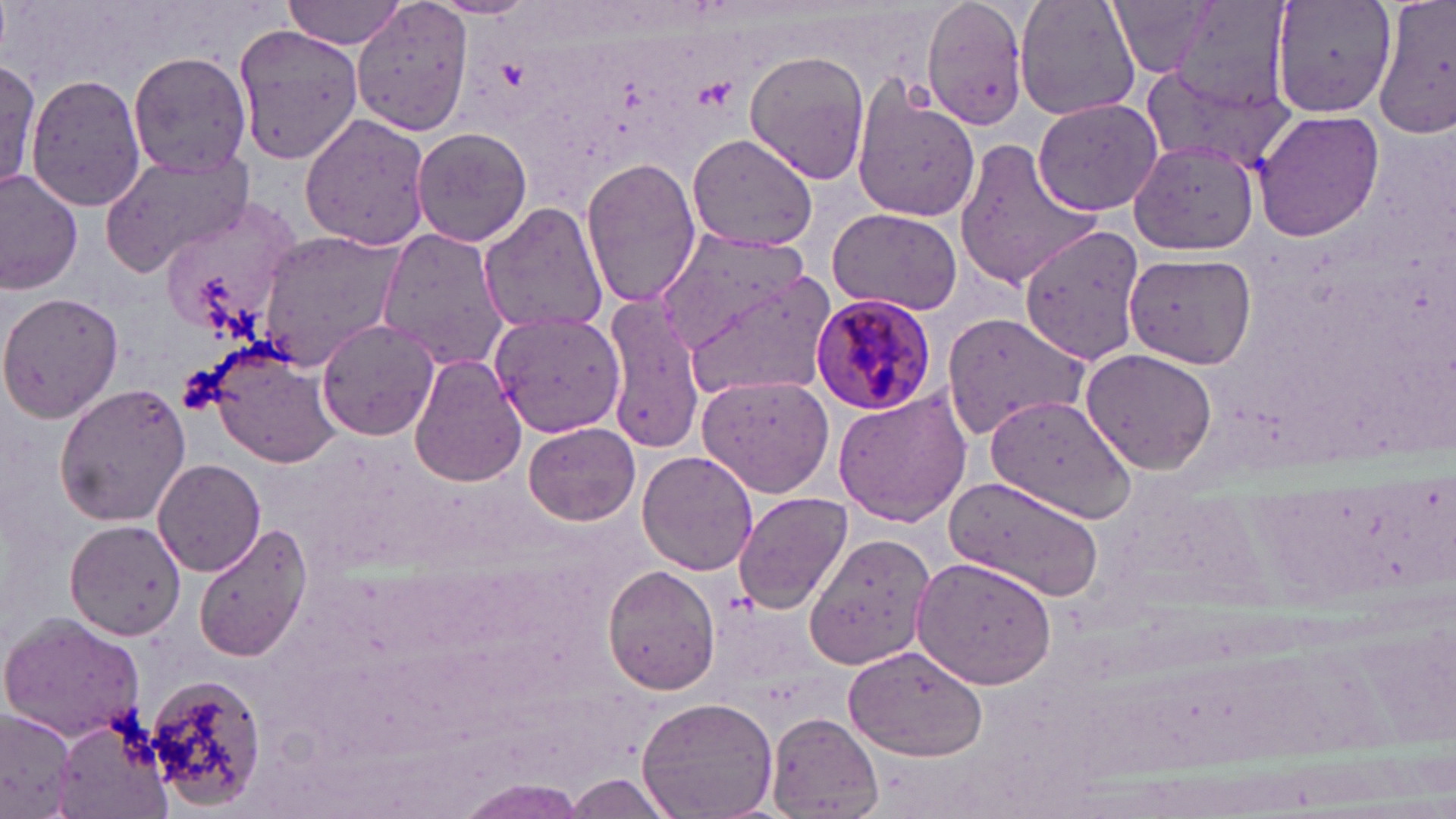
Approximate bounding boxes as [x1, y1, x2, y2] in pixels. Uninfected red blood cell locations: [283, 0, 409, 48], [351, 0, 475, 137], [427, 0, 543, 20], [921, 0, 1030, 128], [1016, 0, 1141, 122], [1108, 0, 1224, 78], [1164, 0, 1295, 117], [1271, 0, 1397, 117], [1371, 1, 1456, 135], [232, 24, 363, 162], [127, 51, 251, 175], [745, 52, 872, 183], [0, 57, 42, 192], [1140, 58, 1294, 178], [25, 73, 145, 213], [853, 88, 982, 224], [1032, 97, 1166, 216], [1252, 110, 1385, 243], [299, 113, 432, 252], [410, 127, 531, 246], [687, 133, 818, 250], [952, 136, 1101, 292], [1125, 141, 1259, 256], [99, 145, 255, 277], [581, 156, 702, 311], [0, 174, 82, 295], [159, 198, 299, 343], [478, 202, 609, 337], [827, 208, 962, 315], [651, 225, 818, 360], [1019, 225, 1148, 363], [254, 228, 406, 371], [376, 228, 510, 367], [1125, 248, 1258, 370], [678, 270, 833, 398], [0, 291, 125, 426], [601, 297, 706, 454], [489, 309, 625, 439], [940, 310, 1088, 440], [316, 317, 442, 441], [208, 345, 341, 468], [1080, 349, 1218, 473], [409, 354, 525, 487], [698, 375, 836, 497], [54, 383, 193, 525], [832, 387, 974, 527], [985, 393, 1135, 525], [524, 422, 638, 525], [637, 450, 758, 574], [152, 459, 265, 576], [945, 474, 1106, 598], [731, 491, 852, 612], [65, 518, 186, 641], [192, 523, 309, 663], [803, 532, 934, 671], [909, 555, 1058, 690], [602, 564, 720, 694], [0, 613, 146, 741], [844, 644, 990, 763], [143, 672, 267, 812], [637, 696, 778, 819], [0, 706, 80, 818], [769, 714, 882, 816], [54, 715, 170, 819], [566, 773, 675, 816], [458, 781, 588, 816]. Plasmodium malariae-infected red blood cell locations: [812, 293, 937, 417]. Slide-level diagnosis: Plasmodium malariae. Image is 1456×819 pixels. Thin blood film. Single field of view. 1000x magnification. May-Grünwald-Giemsa stain. Light microscopy.